Classify this cell by malaria status.
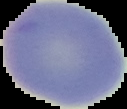
Uninfected.

preparation = thin blood film
image size = 127×109 pixels
image type = segmented cell region with the area outside set to black